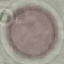

malaria status = uninfected
preparation = thin blood smear
stain = Giemsa
capture = smartphone through the microscope eyepiece
image type = cell patch, automatically extracted from a larger field of view and resized to 64 × 64 pixels